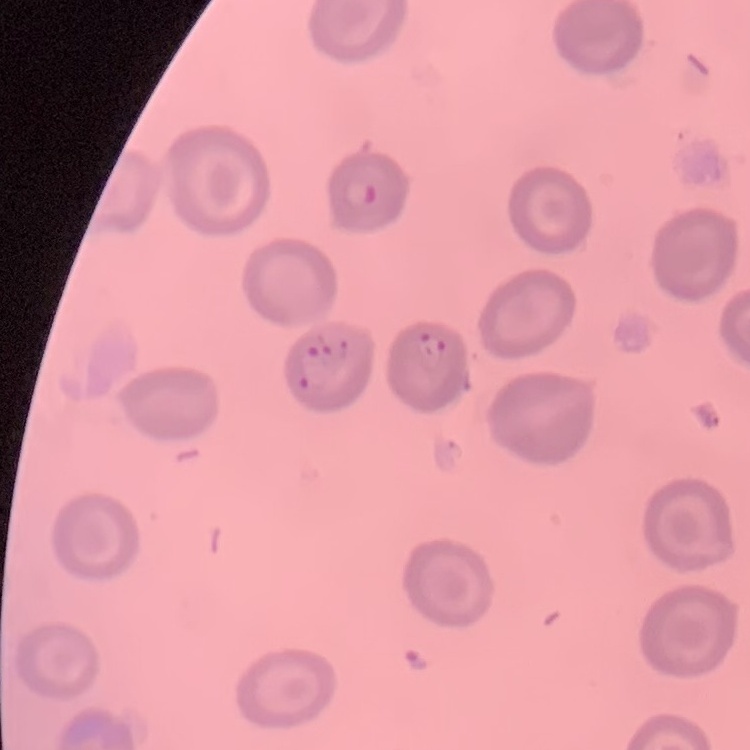
{
  "erythrocyte_morphology": "no rouleaux formation",
  "preparation": "thin peripheral smear",
  "stain": "Field's or Giemsa",
  "image_type": "square crop of a larger photomicrograph"
}